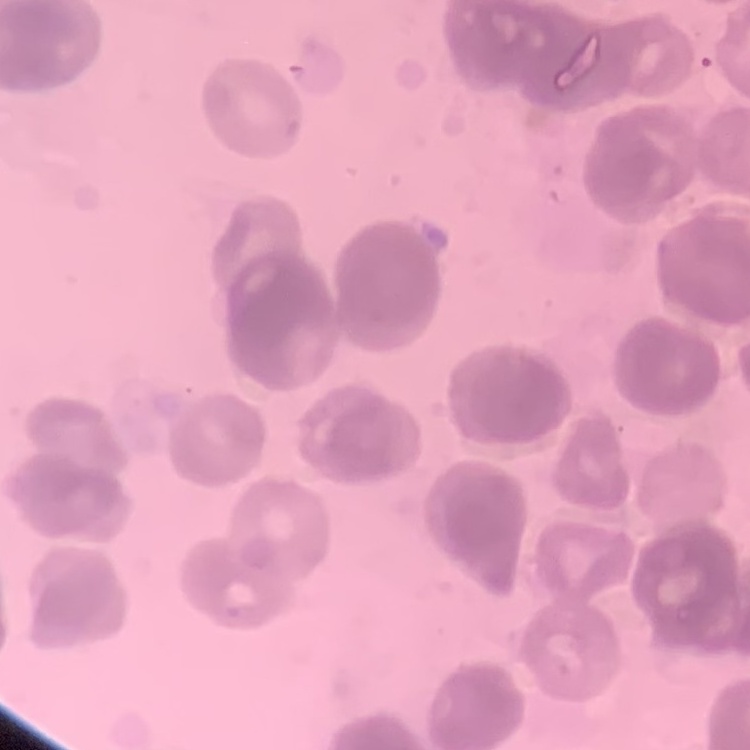
Summary:
  - Erythrocyte morphology: rouleaux formation
  - Preparation: thin peripheral smear
  - Image type: square crop of a larger photomicrograph
  - Stain: Field's or Giemsa